Outline each blood parasite and name the species.
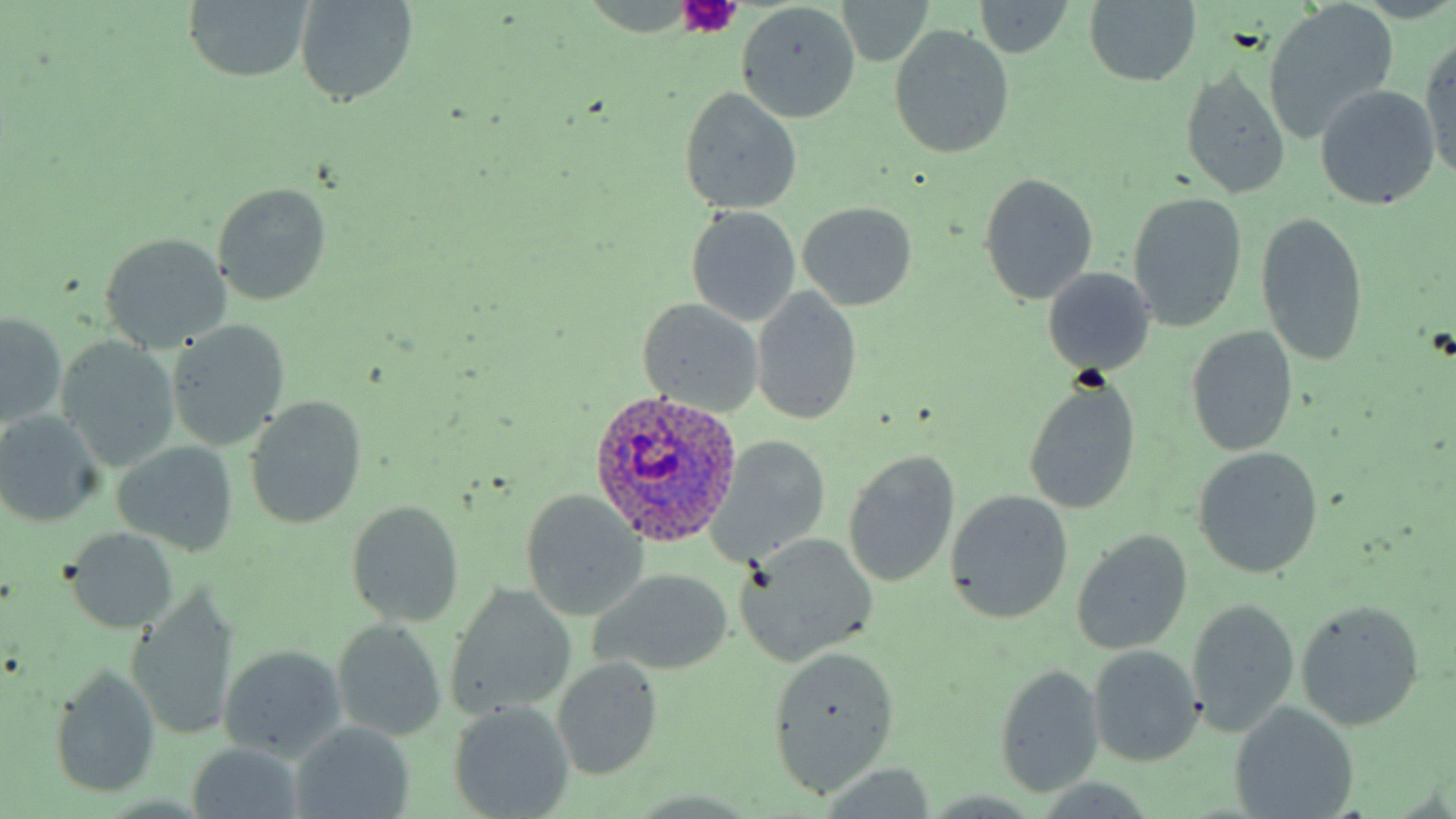
Approximate bounding boxes as [x1, y1, x2, y2] in pixels.
Plasmodium ovale-infected red blood cells: [587, 387, 743, 545].
No Plasmodium falciparum, Plasmodium malariae, Plasmodium vivax, Babesia divergens, or Trypanosoma brucei observed.

Uninfected red blood cell locations: [181, 0, 315, 84], [294, 0, 419, 107], [1082, 0, 1203, 88], [971, 1, 1072, 58], [835, 2, 936, 67], [736, 3, 862, 123], [1264, 3, 1401, 143], [888, 24, 1014, 160], [1419, 35, 1456, 184], [1178, 65, 1292, 200], [1313, 84, 1442, 210], [677, 87, 803, 216], [979, 172, 1099, 305], [211, 181, 334, 306], [1126, 192, 1248, 333], [796, 201, 919, 310], [685, 206, 802, 326], [1254, 212, 1370, 369], [97, 233, 233, 352], [1041, 267, 1156, 377], [751, 287, 863, 425], [636, 298, 766, 416], [1, 311, 68, 428], [164, 321, 291, 451], [1184, 326, 1299, 458], [55, 336, 181, 471], [1023, 376, 1141, 515], [242, 396, 370, 530], [0, 410, 106, 527], [713, 435, 832, 562], [111, 439, 241, 558], [1191, 447, 1325, 579], [842, 449, 961, 589], [944, 489, 1075, 625], [518, 490, 651, 622], [345, 499, 465, 628], [61, 526, 181, 634], [1070, 529, 1193, 654], [735, 533, 879, 667], [587, 568, 736, 678], [445, 585, 577, 718], [127, 591, 241, 741], [1185, 597, 1299, 738], [1294, 598, 1427, 731], [331, 618, 449, 743], [763, 642, 900, 798], [217, 644, 349, 763], [1087, 644, 1205, 767], [551, 655, 665, 781], [49, 663, 162, 801], [993, 664, 1104, 798], [447, 702, 576, 818], [1230, 702, 1360, 818], [289, 723, 416, 818], [184, 742, 309, 818]. Platelet locations: [676, 0, 743, 35]. Slide-level diagnosis: Plasmodium ovale. Image is 1456×819 pixels. Thin blood smear. Captured at 1000x magnification. May-Grünwald-Giemsa stain. Light microscopy. One field of a larger specimen.